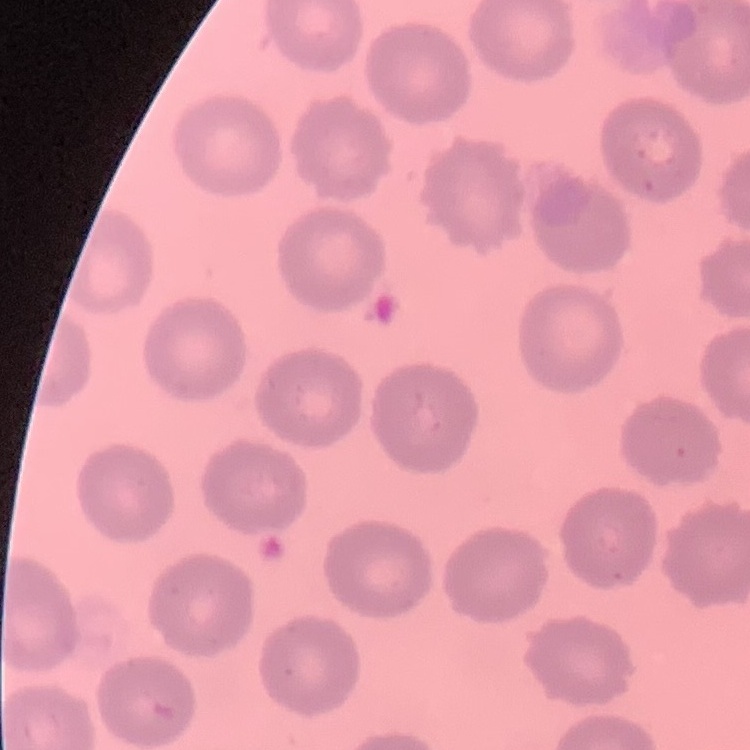

{
  "erythrocyte_morphology": "no rouleaux formation",
  "stain": "Field's or Giemsa",
  "preparation": "thin blood film",
  "image_type": "one tile cut from a larger photomicrograph"
}